Point out each malaria parasite.
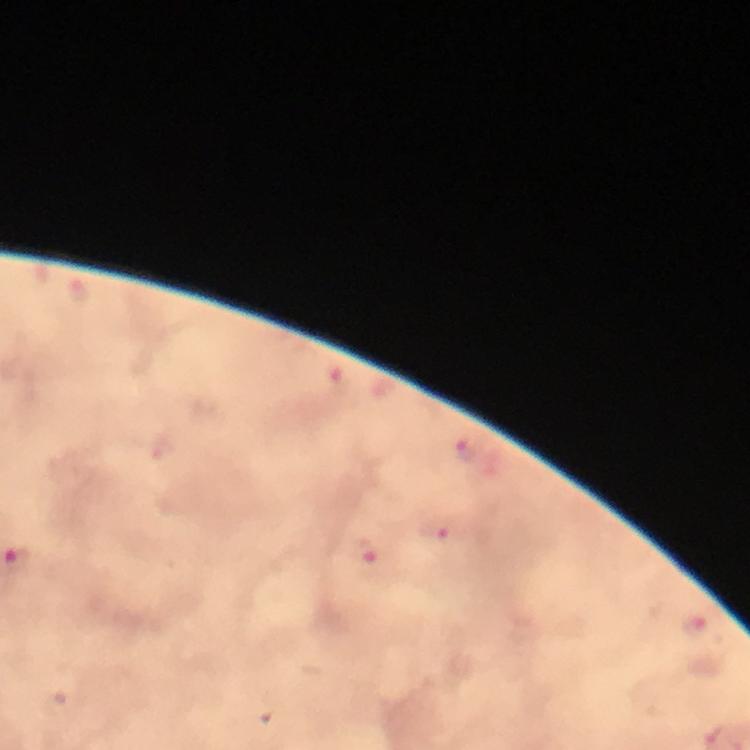
Approximate centers as {x, y} in pixels.
Malaria parasites: {80, 292}, {467, 446}, {437, 530}, {363, 552}, {693, 624}.

image size = 750×750 pixels
preparation = thick blood film
magnification = 100x
immersion oil = applied
capture = smartphone camera through the microscope
stain = Giemsa
cropped from = one field of view
context = from a diagnostic examination for malaria